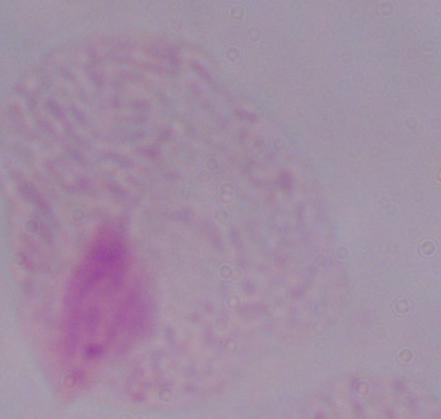

Captured at 1000x magnification. Micrograph. A trichomonad is seen.